Classify this cell by malaria status.
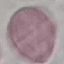
It is uninfected.

Summary:
  - Preparation: thin smear
  - Image type: cell patch, automatically extracted from a larger field of view and resized to 64 × 64 pixels
  - Capture: smartphone camera at the microscope eyepiece
  - Stain: Giemsa